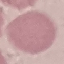

Result: negative for malaria parasites. Giemsa stain. Acquired by smartphone through the microscope eyepiece. Cell patch, automatically extracted from a larger field of view and resized to 64 × 64 pixels. Thin smear of blood.